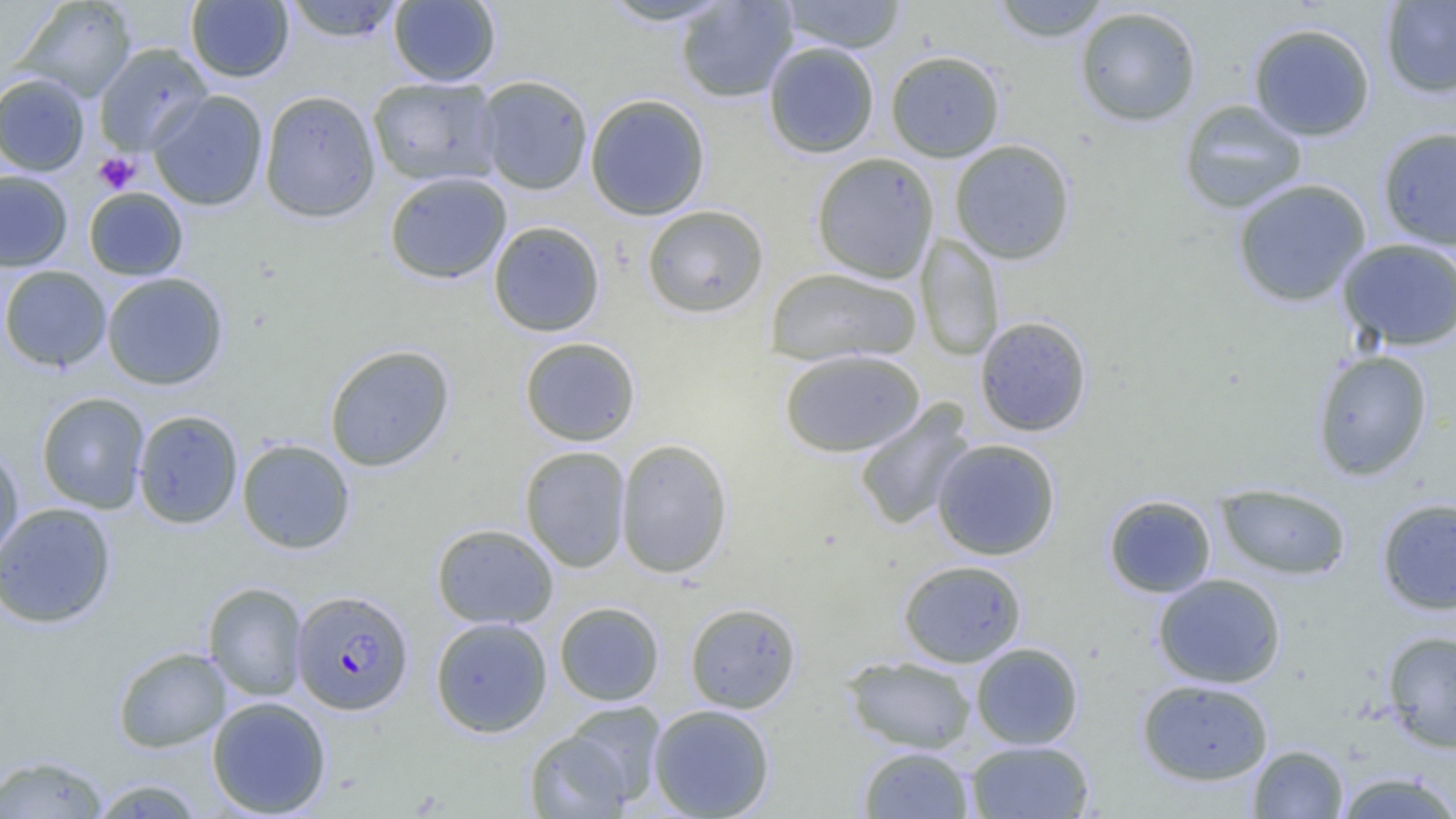

Summary:
  - Coordinate format: approximate bounding boxes as named x1/y1/x2/y2 corners in pixels
  - Uninfected red blood cell locations: (x1=281, y1=0, x2=406, y2=42), (x1=388, y1=0, x2=501, y2=87), (x1=598, y1=0, x2=735, y2=27), (x1=675, y1=0, x2=798, y2=103), (x1=780, y1=0, x2=907, y2=53), (x1=990, y1=0, x2=1114, y2=42), (x1=16, y1=1, x2=137, y2=102), (x1=186, y1=1, x2=294, y2=82), (x1=1380, y1=1, x2=1456, y2=98), (x1=1074, y1=5, x2=1203, y2=127), (x1=1248, y1=22, x2=1376, y2=141), (x1=763, y1=42, x2=880, y2=158), (x1=94, y1=43, x2=213, y2=156), (x1=885, y1=50, x2=1005, y2=162), (x1=0, y1=73, x2=90, y2=176), (x1=476, y1=75, x2=593, y2=195), (x1=367, y1=76, x2=503, y2=187), (x1=149, y1=90, x2=268, y2=211), (x1=259, y1=90, x2=380, y2=222), (x1=584, y1=94, x2=711, y2=220), (x1=1178, y1=99, x2=1308, y2=214), (x1=1377, y1=126, x2=1456, y2=250), (x1=949, y1=139, x2=1076, y2=264), (x1=811, y1=152, x2=939, y2=283), (x1=0, y1=170, x2=73, y2=272), (x1=384, y1=171, x2=512, y2=284), (x1=1232, y1=178, x2=1372, y2=307), (x1=84, y1=188, x2=189, y2=280), (x1=641, y1=204, x2=769, y2=318), (x1=489, y1=221, x2=605, y2=337), (x1=916, y1=233, x2=1005, y2=361), (x1=1337, y1=238, x2=1456, y2=351), (x1=0, y1=265, x2=111, y2=372), (x1=765, y1=268, x2=922, y2=366), (x1=101, y1=272, x2=228, y2=390), (x1=974, y1=316, x2=1092, y2=437), (x1=520, y1=337, x2=641, y2=446), (x1=324, y1=344, x2=455, y2=472), (x1=779, y1=349, x2=925, y2=458), (x1=1311, y1=349, x2=1433, y2=481), (x1=36, y1=392, x2=150, y2=514), (x1=853, y1=401, x2=976, y2=531), (x1=132, y1=409, x2=243, y2=529), (x1=616, y1=438, x2=733, y2=579), (x1=931, y1=438, x2=1061, y2=560), (x1=237, y1=439, x2=355, y2=554), (x1=519, y1=445, x2=631, y2=572), (x1=0, y1=446, x2=25, y2=569), (x1=1215, y1=483, x2=1352, y2=581), (x1=1103, y1=494, x2=1216, y2=598), (x1=1377, y1=497, x2=1456, y2=615), (x1=0, y1=502, x2=117, y2=629), (x1=431, y1=523, x2=558, y2=629), (x1=897, y1=560, x2=1027, y2=668), (x1=1152, y1=573, x2=1286, y2=688), (x1=203, y1=582, x2=309, y2=701), (x1=554, y1=601, x2=665, y2=706), (x1=685, y1=601, x2=801, y2=713), (x1=430, y1=616, x2=552, y2=737), (x1=1382, y1=630, x2=1456, y2=753), (x1=970, y1=642, x2=1083, y2=750), (x1=113, y1=646, x2=230, y2=753), (x1=842, y1=655, x2=977, y2=754), (x1=1136, y1=678, x2=1274, y2=786), (x1=206, y1=696, x2=332, y2=817), (x1=562, y1=701, x2=666, y2=804), (x1=648, y1=704, x2=775, y2=818), (x1=524, y1=728, x2=633, y2=818), (x1=964, y1=739, x2=1095, y2=819), (x1=1248, y1=744, x2=1348, y2=818), (x1=858, y1=745, x2=974, y2=818), (x1=1, y1=753, x2=109, y2=818), (x1=1333, y1=771, x2=1456, y2=818), (x1=87, y1=777, x2=205, y2=818)
  - Platelet locations: (x1=93, y1=152, x2=141, y2=194)
  - Plasmodium falciparum-infected red blood cell locations: (x1=290, y1=589, x2=414, y2=715)
  - Slide-level diagnosis: Plasmodium falciparum
  - Modality: optical microscopy
  - Magnification: 1000x
  - Image size: 1456×819 pixels
  - Preparation: thin blood smear
  - Field of view: single